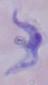
{
  "identification": "trypanosome",
  "modality": "photomicrograph",
  "magnification": "1000x"
}